Classify this cell by malaria status.
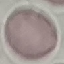
It is uninfected.

Summary:
  - Capture: smartphone through the microscope eyepiece
  - Image type: automatically extracted cell patch, resized to 64 × 64 pixels
  - Preparation: thin blood film
  - Stain: Giemsa